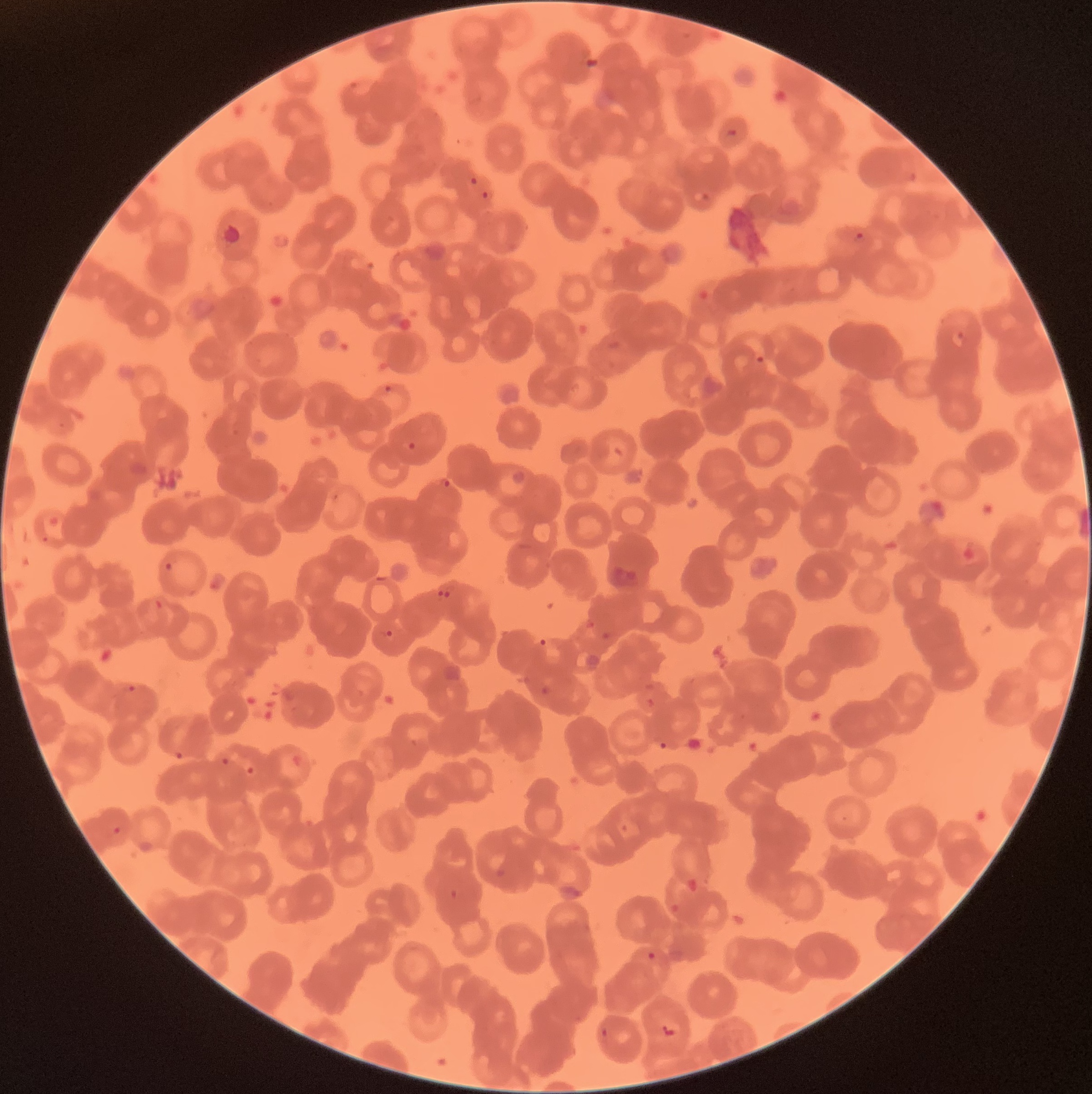

Summary:
  - Coordinate format: approximate bounding boxes as [x1, y1, x2, y2] in pixels
  - Plasmodium parasite locations: [468, 176, 480, 187], [480, 190, 491, 201], [853, 232, 867, 243], [365, 258, 376, 273], [755, 355, 766, 365], [383, 384, 394, 394], [407, 440, 417, 451], [442, 478, 452, 489], [163, 561, 174, 572], [435, 583, 444, 597], [444, 583, 453, 598], [374, 627, 393, 638], [538, 637, 549, 648], [109, 685, 137, 697], [220, 756, 230, 766], [246, 765, 255, 775], [110, 824, 124, 836], [557, 885, 583, 900], [647, 951, 657, 960], [661, 1023, 678, 1037], [597, 1028, 610, 1038]
  - Preparation: thin blood film
  - Red blood cell morphology: rouleaux formation
  - Modality: optical microscopy
  - Image size: 1092×1094 pixels